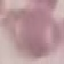

Summary:
  - Malaria status: uninfected
  - Capture: smartphone camera at the microscope eyepiece
  - Image type: automatically extracted cell patch, resized to 64 × 64 pixels
  - Stain: Giemsa
  - Preparation: thin blood smear